Assess this cell for malaria.
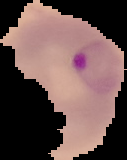

It is parasitized.

preparation = thin blood smear
image size = 127×160 pixels
image type = segmented cell region on a black background